Give the position of every malaria parasite.
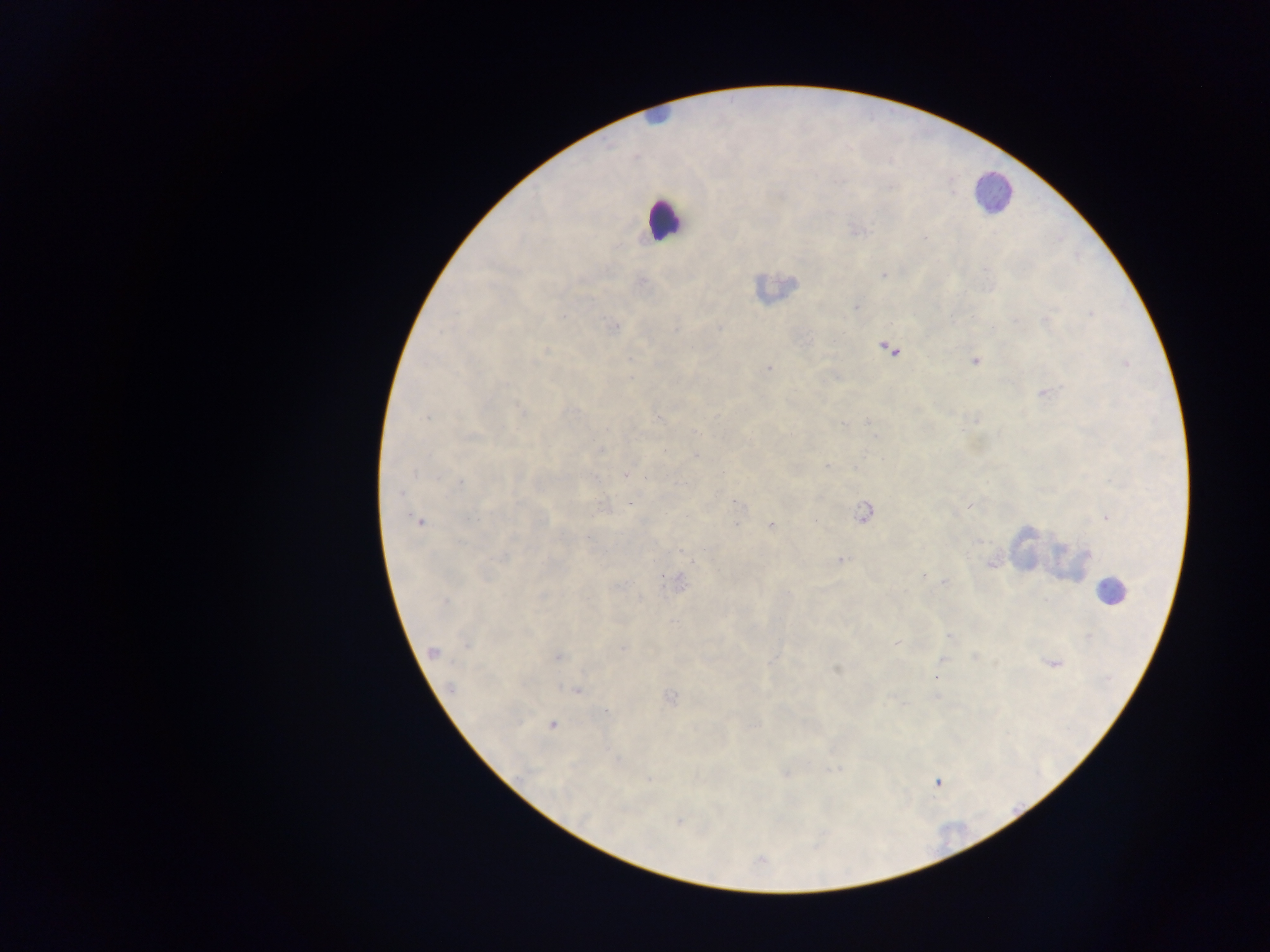

Approximate centers as x y in pixels.
Malaria parasites: 857 230; 925 236; 883 274; 793 283; 856 307; 1090 313; 561 315; 1045 319; 610 327; 674 327; 719 327; 882 345; 545 351; 975 360; 768 368; 629 378; 1046 392; 520 408; 427 417; 657 419; 868 423; 844 424; 971 441; 601 451; 694 454; 829 466; 415 470; 626 474; 462 482; 400 494; 736 506; 864 512; 1106 515; 412 518; 815 520; 419 522; 735 522; 772 526; 978 541; 841 559; 692 560; 991 563; 922 575; 663 580; 672 581; 944 582; 616 585; 787 593; 541 595; 445 602; 949 636; 898 643; 466 644; 623 648; 431 652; 556 656; 974 656; 772 660; 1054 662; 835 670; 936 677; 448 686; 574 689; 669 698; 608 710; 549 725; 617 759; 837 768; 785 774; 648 780; 935 780; 678 822.

Leukocyte locations: 994 190; 668 221; 1113 589. Photographed through a microscope with a mobile-phone camera. Single field of view. Sample from Ghana. Image is 1270×952 pixels. Thick blood film.